Classify this cell by malaria status.
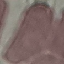
Uninfected.

Summary:
  - Stain: Giemsa
  - Capture: smartphone camera at the microscope eyepiece
  - Image type: automatically extracted cell patch, resized to 64 × 64 pixels
  - Preparation: thin blood film